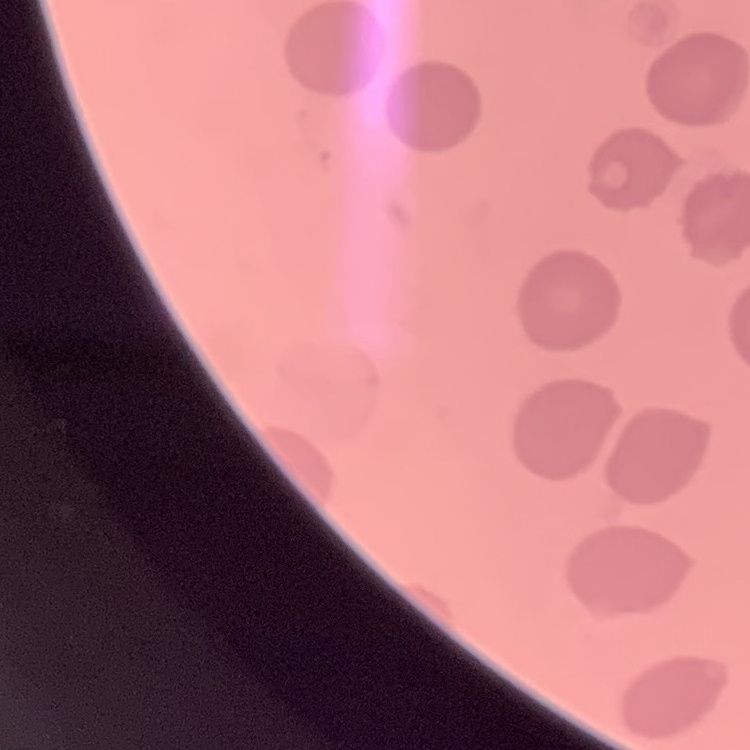 The red blood cells exhibit no rouleaux formation. Thin blood film. Square crop of a larger photomicrograph. Stained with either Field's or Giemsa.